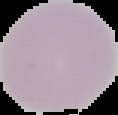
Image is 118×115 pixels. Segmented cell region on a black background. From a thin blood smear. Malaria status: uninfected.